Identify the cell.
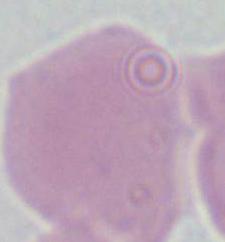
This is an erythrocyte.

modality = micrograph
magnification = 1000x